Outline each Plasmodium falciparum-infected red blood cell.
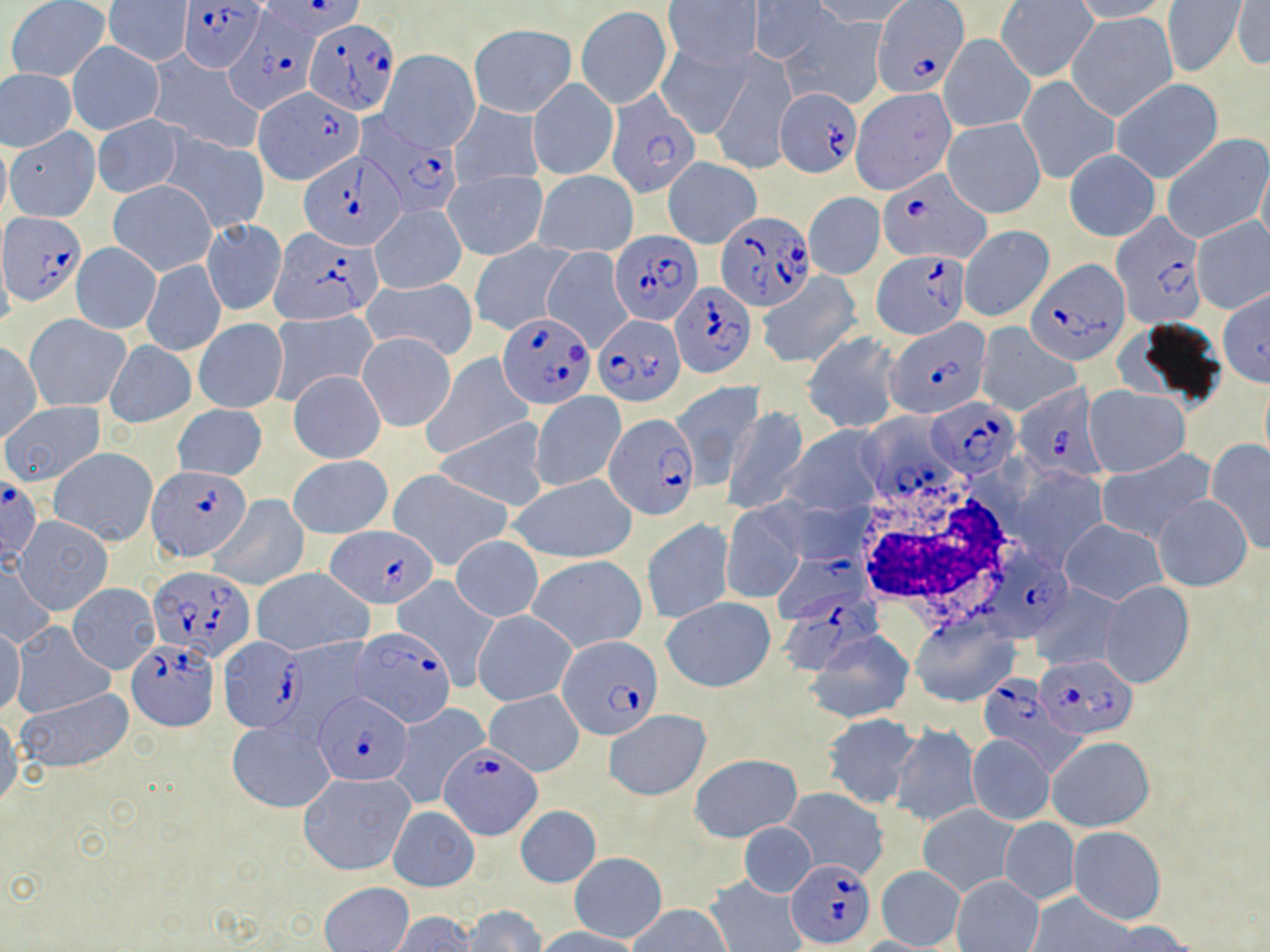
Approximate bounding boxes as (x1, y1, x2, y2) in pixels.
Plasmodium falciparum-infected red blood cells (subset): (262, 0, 364, 39), (179, 1, 265, 72), (873, 1, 968, 97), (225, 14, 322, 114), (305, 18, 398, 116), (775, 88, 862, 179), (605, 90, 699, 198), (363, 123, 462, 216), (299, 150, 407, 249), (878, 171, 988, 263), (717, 211, 817, 311), (2, 214, 85, 306), (1111, 214, 1208, 329), (270, 228, 382, 325), (610, 230, 701, 324), (873, 249, 971, 336), (1025, 257, 1129, 366), (669, 281, 757, 379), (497, 313, 597, 409), (593, 314, 686, 406), (885, 320, 990, 419), (1013, 383, 1108, 481), (928, 399, 1018, 476), (604, 413, 699, 519), (148, 468, 253, 562), (0, 477, 41, 561), (327, 525, 437, 607), (992, 548, 1077, 639), (769, 554, 866, 623), (147, 566, 256, 665), (779, 588, 882, 680), (347, 628, 451, 726), (557, 636, 664, 740), (217, 638, 307, 734), (128, 639, 217, 731), (1036, 654, 1139, 739), (975, 678, 1078, 776), (315, 692, 410, 784), (439, 741, 539, 840), (785, 859, 877, 948).

White blood cell locations: (849, 470, 1025, 626). Uninfected red blood cell locations (subset): (664, 0, 761, 68), (1069, 0, 1173, 22), (5, 1, 110, 80), (106, 1, 193, 65), (814, 1, 919, 27), (994, 1, 1098, 82), (1160, 1, 1249, 78), (751, 2, 831, 64), (1232, 2, 1269, 70), (576, 5, 672, 109), (1066, 12, 1177, 122), (782, 16, 888, 110), (469, 23, 577, 116), (940, 35, 1035, 133), (1084, 37, 1196, 160), (67, 41, 163, 134), (657, 44, 752, 140), (379, 49, 481, 152), (707, 50, 796, 174), (146, 52, 265, 155), (1, 71, 77, 150), (1017, 75, 1120, 185), (528, 79, 618, 181), (1112, 79, 1224, 183), (256, 88, 358, 183), (851, 88, 955, 194), (450, 100, 544, 191), (93, 115, 184, 198), (942, 116, 1045, 219), (90, 121, 260, 213), (5, 127, 100, 222), (161, 132, 270, 233), (1161, 133, 1269, 243), (0, 135, 11, 223), (1064, 149, 1160, 241), (1256, 155, 1270, 254), (663, 157, 761, 247), (444, 168, 549, 260), (534, 170, 638, 257), (108, 179, 216, 277), (805, 193, 884, 280), (371, 205, 465, 294), (1191, 216, 1270, 314), (201, 218, 287, 317), (957, 225, 1053, 322), (470, 239, 575, 334), (71, 243, 161, 333), (0, 248, 15, 337), (140, 258, 227, 358), (757, 272, 860, 367), (361, 276, 478, 360), (1216, 286, 1269, 389), (266, 309, 378, 404), (1116, 313, 1232, 416), (27, 315, 129, 411), (194, 319, 288, 413), (975, 324, 1079, 416), (803, 331, 902, 433), (357, 332, 456, 431), (104, 340, 196, 428), (0, 342, 42, 442), (424, 353, 534, 459), (288, 370, 386, 463), (670, 381, 764, 484), (1083, 386, 1189, 476), (530, 391, 625, 491), (2, 401, 105, 487), (173, 404, 267, 480), (722, 405, 809, 515), (858, 413, 964, 506), (434, 417, 549, 512), (782, 424, 891, 517), (1206, 439, 1270, 554), (49, 448, 157, 546), (1096, 450, 1214, 543), (290, 455, 393, 540), (1007, 467, 1109, 567), (388, 470, 511, 571), (508, 474, 638, 564), (209, 494, 307, 590), (1153, 495, 1253, 590), (720, 503, 806, 604), (16, 516, 113, 615), (643, 519, 734, 624), (1061, 520, 1165, 605), (449, 534, 543, 621), (526, 555, 648, 652), (1, 563, 56, 649), (251, 567, 373, 656), (393, 576, 499, 684), (1099, 581, 1193, 687), (67, 582, 159, 673), (1027, 583, 1125, 671), (661, 597, 776, 692), (473, 610, 576, 706), (910, 617, 1018, 706), (9, 621, 114, 719), (0, 625, 25, 717), (806, 630, 915, 723), (14, 687, 136, 773), (485, 690, 585, 776), (386, 704, 488, 808), (604, 711, 711, 801), (821, 713, 920, 808), (0, 714, 22, 811), (227, 719, 334, 812), (889, 723, 982, 828), (966, 735, 1055, 826), (1046, 736, 1154, 832), (690, 753, 803, 841), (296, 771, 415, 875), (781, 787, 889, 880), (514, 804, 602, 890), (918, 804, 1019, 896), (388, 805, 479, 891), (999, 818, 1079, 905), (737, 821, 817, 897), (1068, 826, 1165, 925), (569, 852, 666, 944), (877, 866, 965, 948), (705, 874, 806, 952), (951, 876, 1043, 952), (321, 882, 413, 952), (1028, 891, 1136, 950), (628, 904, 731, 952), (462, 905, 545, 952), (389, 913, 475, 952), (1098, 922, 1195, 951), (534, 926, 643, 952). Slide-level diagnosis: Plasmodium falciparum. Light microscopy. Thin blood smear. 1000x magnification. May-Grünwald-Giemsa stain. Single field of view. Image is 1270×952 pixels.